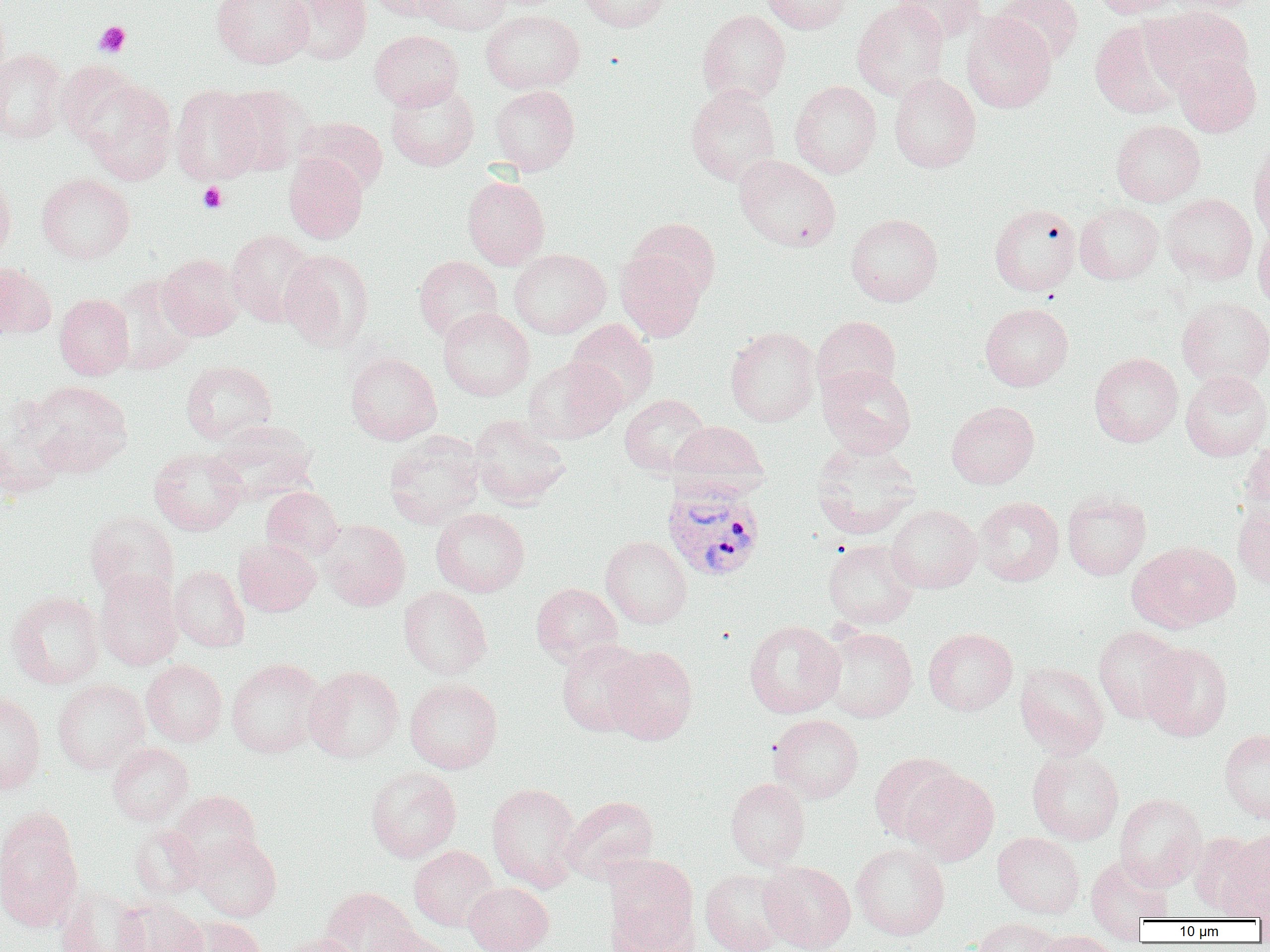

{
  "slide_level_diagnosis": "Plasmodium vivax",
  "preparation": "thin blood film",
  "modality": "light microscopy",
  "platelet_locations": "approximate bounding boxes as (x1,y1)-(x2,y2) corner pairs in pixels: (94,21)-(130,58), (198,182)-(227,213)",
  "magnification": "1000x",
  "uninfected_red_blood_cell_locations": "approximate bounding boxes as (x1,y1)-(x2,y2) corner pairs in pixels: (212,0)-(313,69), (282,0)-(372,64), (368,0)-(454,21), (418,0)-(511,35), (578,0)-(672,32), (762,0)-(852,33), (852,0)-(949,100), (991,0)-(1085,66), (1092,0)-(1185,18), (1165,0)-(1265,13), (892,1)-(987,42), (1144,6)-(1253,93), (480,9)-(584,94), (697,9)-(790,104), (961,13)-(1056,113), (1090,19)-(1187,118), (369,30)-(464,110), (0,49)-(67,143), (1173,53)-(1261,137), (56,64)-(141,146), (889,73)-(981,173), (81,79)-(177,185), (385,81)-(479,171), (790,81)-(882,178), (219,84)-(312,175), (171,85)-(262,184), (489,85)-(580,175), (686,86)-(780,185), (294,116)-(388,194), (1111,120)-(1205,206), (1248,140)-(1270,243), (284,153)-(368,243), (734,154)-(841,252), (0,172)-(16,264), (37,173)-(135,263), (462,175)-(550,269), (1161,193)-(1257,284), (1074,202)-(1163,284), (989,203)-(1081,295), (846,214)-(943,306), (627,217)-(721,302), (1253,225)-(1270,311), (227,230)-(317,326), (280,249)-(374,351), (508,249)-(611,339), (615,249)-(706,342), (157,254)-(245,340), (414,255)-(503,341), (0,263)-(56,339), (110,274)-(199,373), (55,294)-(134,380), (1177,296)-(1270,388), (980,303)-(1074,391), (437,307)-(535,401), (812,316)-(901,400), (566,319)-(659,412), (724,327)-(820,427), (345,352)-(442,445), (1089,352)-(1183,447), (522,357)-(624,444), (181,360)-(276,444), (818,365)-(916,457), (1180,370)-(1270,461), (27,380)-(133,477), (619,394)-(711,478), (947,401)-(1039,488), (0,406)-(68,498), (468,415)-(571,509), (207,420)-(318,506), (669,420)-(769,498), (384,432)-(486,529), (810,440)-(921,539), (1239,440)-(1270,526), (149,448)-(247,535), (261,486)-(344,561), (1062,492)-(1151,580), (975,496)-(1064,586), (1233,503)-(1270,589), (886,504)-(982,593), (431,507)-(530,597), (84,511)-(180,602), (317,518)-(410,611), (600,536)-(692,628), (234,538)-(321,616), (823,539)-(919,629), (1128,540)-(1240,633), (169,565)-(249,652), (95,570)-(183,670), (532,583)-(623,666), (398,585)-(492,679), (7,590)-(105,689), (744,620)-(845,718), (1093,625)-(1185,723), (821,626)-(917,722), (924,628)-(1017,715), (556,639)-(649,737), (1139,643)-(1233,741), (604,646)-(697,745), (226,657)-(326,758), (141,659)-(227,746), (1015,662)-(1110,758), (305,665)-(404,764), (53,679)-(149,774), (404,679)-(503,773), (0,692)-(46,794), (769,714)-(864,802), (1219,729)-(1270,824), (107,742)-(193,825), (1027,747)-(1124,845), (868,752)-(962,844), (366,766)-(462,862), (901,769)-(999,865), (725,778)-(810,870), (486,782)-(582,891), (169,791)-(261,872), (1114,793)-(1206,890), (562,795)-(659,884), (0,813)-(82,933), (130,824)-(205,901), (993,832)-(1084,918), (1214,832)-(1270,919), (192,833)-(281,921), (851,842)-(949,940), (409,845)-(499,931), (1085,854)-(1174,935), (604,856)-(699,951), (759,861)-(856,952), (701,869)-(789,952), (464,881)-(554,952), (56,885)-(148,952), (319,887)-(419,952), (115,898)-(208,952), (178,916)-(267,952), (972,918)-(1059,952), (367,929)-(456,952), (1033,930)-(1118,952), (279,934)-(362,952)",
  "field_of_view": "single",
  "image_size": "1270×952 pixels",
  "plasmodium_vivax_infected_red_blood_cell_locations": "approximate bounding boxes as (x1,y1)-(x2,y2) corner pairs in pixels: (662,482)-(766,582)"
}